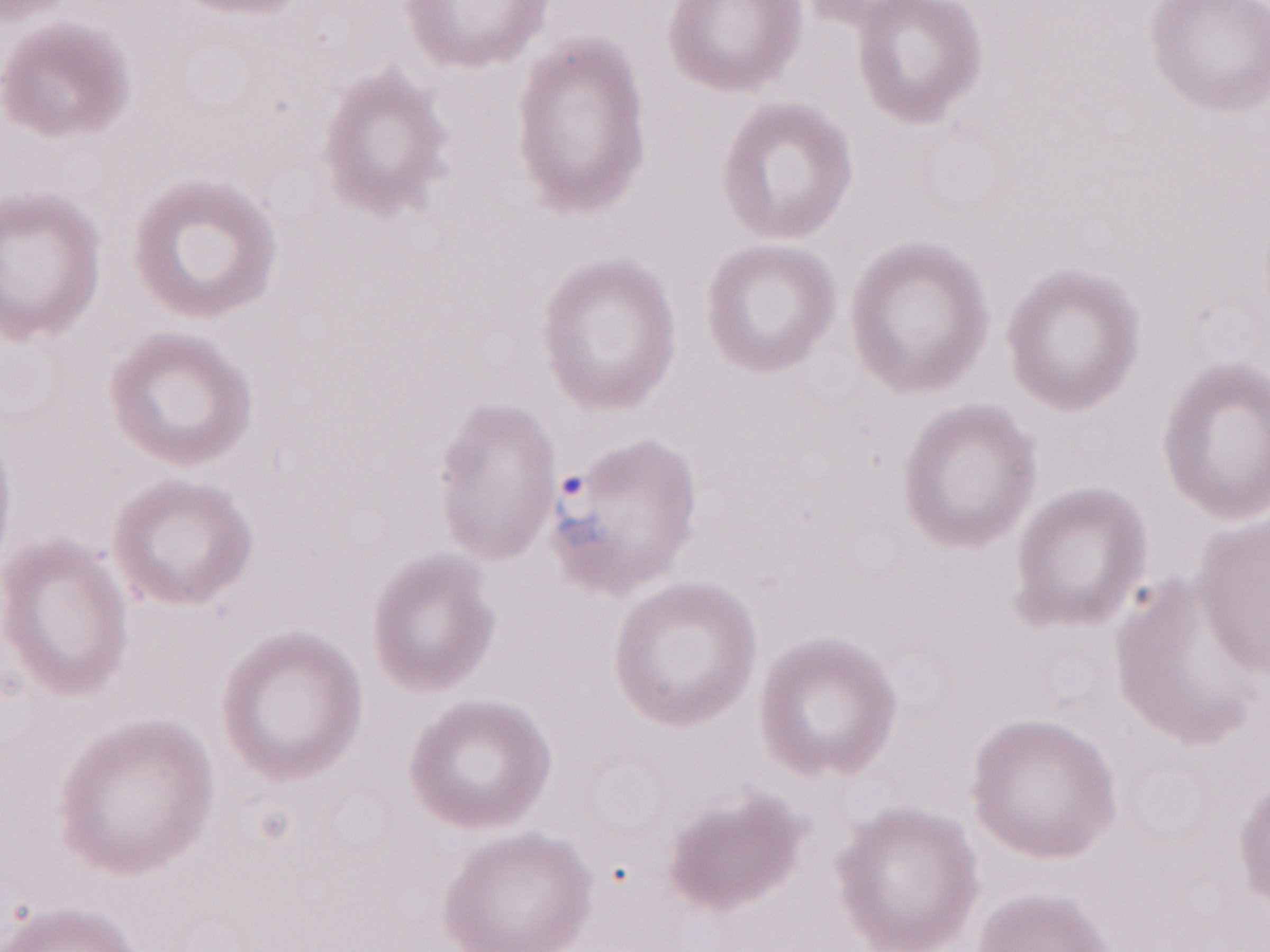
Single field of view. Thin peripheral-blood smear. Patient diagnosis: malaria infection. Magnification: 1,000x. May-Grünwald-Giemsa (MGG) stain. Image is 1270×952 pixels. Olympus BX43 microscope, Olympus DP73 camera.